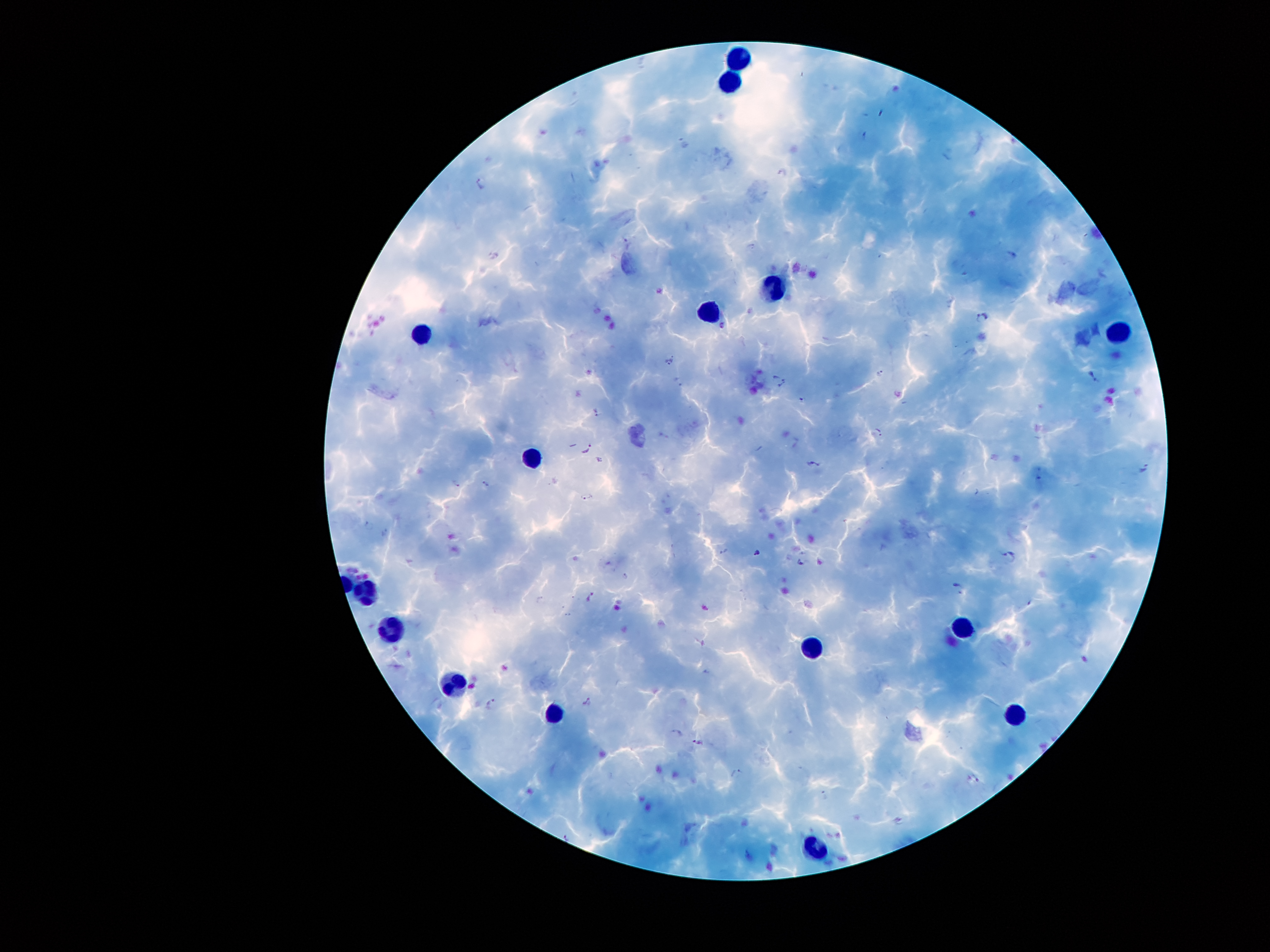

Approximate centers as (x, y) in pixels.
Summary:
  - Leukocyte locations: (742, 51), (729, 77), (774, 287), (710, 308), (1120, 327), (427, 333), (535, 455), (364, 589), (393, 630), (959, 633), (813, 646), (456, 686), (555, 714), (1020, 715), (818, 844)
  - Plasmodium parasite locations: (481, 182), (627, 237), (982, 320), (723, 326), (671, 359), (879, 374), (1092, 375), (778, 380), (801, 400), (595, 412), (879, 433), (586, 448), (814, 463), (1143, 470), (455, 483), (486, 483), (587, 497), (370, 524), (723, 552), (756, 552), (1010, 556), (800, 562), (626, 576), (959, 589), (591, 596), (587, 702), (492, 703), (676, 733), (698, 743), (737, 774), (974, 779), (825, 795), (569, 837)
  - Patient malaria status: positive for Plasmodium falciparum
  - Magnification: 100x
  - Image size: 1270×952 pixels
  - Field of view: one from this slide
  - Capture: smartphone camera through the microscope eyepiece
  - Stain: Giemsa
  - Preparation: thick blood smear